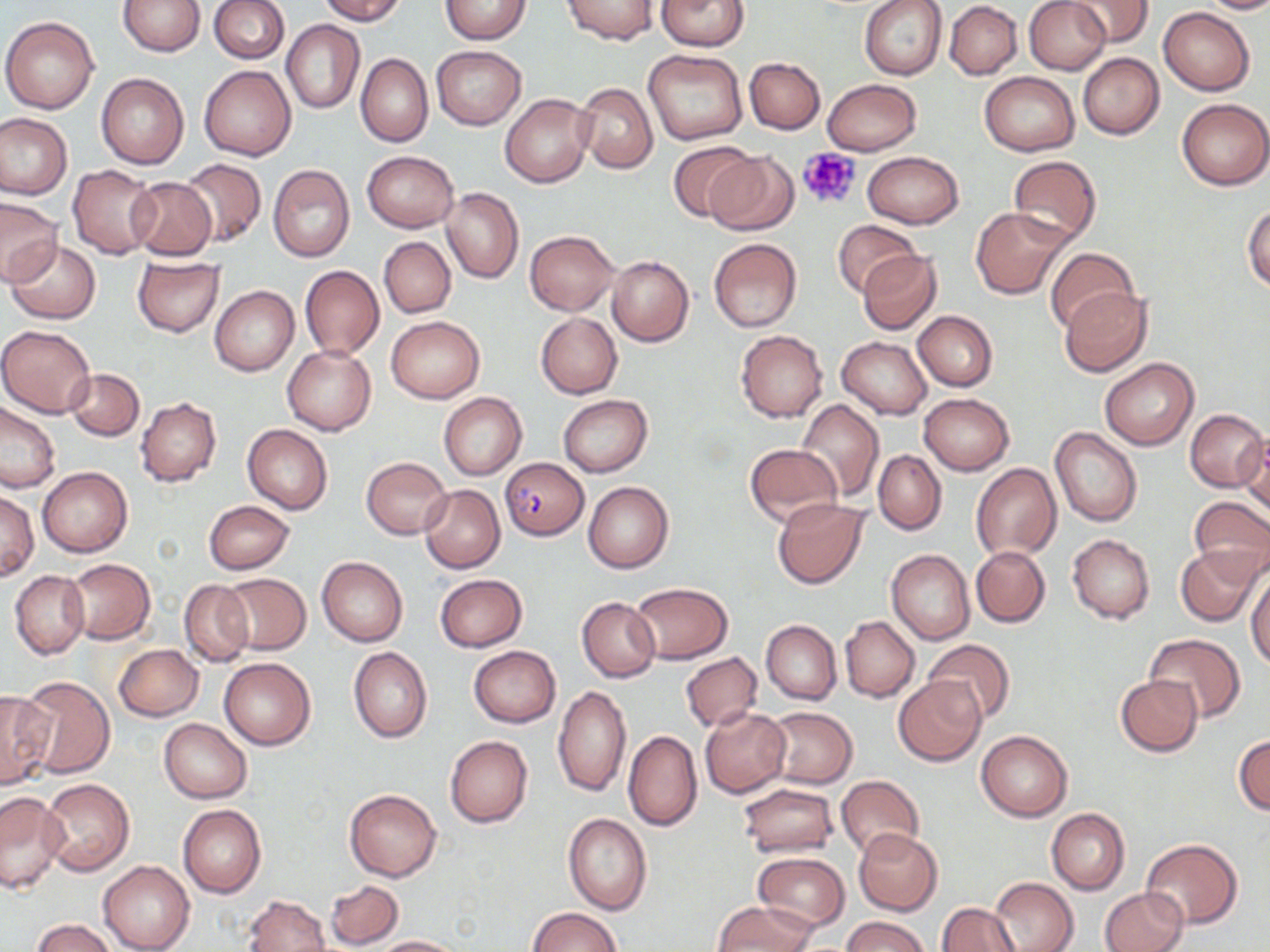

slide-level diagnosis = Plasmodium falciparum
field of view = single
Plasmodium falciparum-infected red blood cell locations = approximate bounding boxes as (x1, y1, x2, y2) in pixels: (501, 455, 588, 541)
modality = optical microscopy
preparation = thin blood film
uninfected red blood cell locations = approximate bounding boxes as (x1, y1, x2, y2) in pixels: (117, 0, 205, 56), (208, 0, 289, 63), (317, 0, 405, 24), (440, 0, 533, 44), (562, 0, 658, 45), (656, 0, 751, 50), (859, 0, 948, 80), (1025, 0, 1110, 74), (1067, 0, 1153, 46), (1199, 0, 1270, 14), (945, 2, 1022, 79), (1159, 8, 1255, 96), (1, 16, 99, 113), (281, 19, 363, 114), (432, 45, 526, 130), (643, 48, 748, 145), (355, 52, 432, 146), (1078, 54, 1164, 140), (745, 57, 825, 133), (200, 65, 297, 160), (979, 72, 1080, 156), (96, 73, 189, 169), (822, 79, 922, 156), (574, 82, 659, 173), (500, 94, 594, 187), (1177, 98, 1270, 190), (0, 114, 71, 198), (668, 140, 760, 223), (704, 151, 798, 235), (862, 151, 964, 228), (362, 152, 459, 232), (1007, 155, 1102, 245), (179, 159, 266, 247), (267, 163, 356, 262), (68, 165, 161, 259), (125, 177, 218, 260), (441, 187, 523, 284), (1, 199, 61, 285), (1243, 204, 1270, 291), (970, 207, 1070, 299), (832, 218, 922, 298), (525, 230, 619, 315), (379, 237, 455, 318), (708, 238, 802, 332), (7, 240, 102, 324), (1046, 246, 1137, 333), (856, 249, 944, 336), (131, 256, 225, 338), (607, 256, 694, 346), (298, 266, 385, 360), (210, 286, 299, 375), (1060, 286, 1153, 376), (913, 311, 997, 392), (535, 312, 622, 398), (386, 315, 486, 404), (0, 324, 97, 417), (736, 330, 828, 422), (837, 337, 932, 420), (283, 345, 376, 435), (1099, 358, 1199, 450), (66, 368, 144, 441), (437, 392, 527, 480), (918, 393, 1014, 475), (558, 395, 652, 477), (136, 397, 221, 487), (794, 399, 885, 501), (0, 402, 62, 494), (1185, 408, 1268, 492), (243, 425, 333, 514), (1050, 426, 1143, 526), (1240, 434, 1269, 515), (743, 444, 843, 529), (873, 450, 947, 536), (362, 456, 450, 539), (972, 464, 1061, 560), (39, 466, 132, 558), (584, 481, 674, 573), (420, 484, 504, 573), (1, 490, 38, 582), (1188, 496, 1270, 585), (773, 498, 868, 588), (203, 500, 295, 574), (1068, 533, 1155, 623), (971, 545, 1049, 627), (1176, 546, 1262, 627), (887, 549, 974, 644), (317, 558, 408, 645), (65, 559, 155, 644), (11, 571, 89, 659), (1247, 572, 1270, 668), (220, 574, 311, 654), (434, 574, 527, 651), (180, 580, 253, 666), (629, 582, 733, 664), (577, 596, 660, 682), (839, 616, 919, 702), (760, 620, 842, 704), (1146, 634, 1245, 723), (924, 638, 1014, 725), (115, 644, 203, 721), (468, 646, 561, 727), (349, 647, 432, 742), (680, 653, 762, 732), (220, 657, 316, 750), (1115, 674, 1203, 756), (18, 676, 115, 779), (894, 676, 986, 766), (553, 685, 632, 798), (0, 691, 54, 789), (766, 706, 856, 788), (700, 708, 792, 798), (159, 719, 252, 803), (624, 730, 702, 831), (975, 730, 1072, 821), (1233, 733, 1270, 815), (445, 735, 533, 827), (835, 774, 924, 859), (41, 778, 135, 877), (739, 783, 839, 857), (344, 787, 442, 882), (0, 790, 69, 894), (178, 805, 266, 898), (1046, 808, 1130, 895), (562, 812, 652, 916), (853, 828, 943, 916), (1140, 838, 1242, 929), (754, 851, 849, 931), (98, 860, 194, 952), (990, 877, 1078, 952), (326, 880, 404, 949), (1100, 888, 1187, 951), (243, 894, 330, 952), (712, 901, 815, 951), (936, 903, 1020, 952), (529, 908, 620, 952), (843, 916, 930, 952), (32, 918, 117, 952), (375, 935, 465, 951)
magnification = 1000x
image size = 1270×952 pixels
platelet locations = approximate bounding boxes as (x1, y1, x2, y2) in pixels: (797, 146, 864, 211)
stain = May-Grünwald-Giemsa